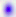
Summary:
  - Modality: micrograph
  - Magnification: 400x
  - Identification: Toxoplasma gondii